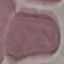

Summary:
  - Malaria status: uninfected
  - Preparation: thin blood smear
  - Stain: Giemsa
  - Capture: smartphone camera at the microscope eyepiece
  - Image type: cell patch, automatically extracted from a larger field of view and resized to 64 × 64 pixels